Assess the morphology of the red blood cells.
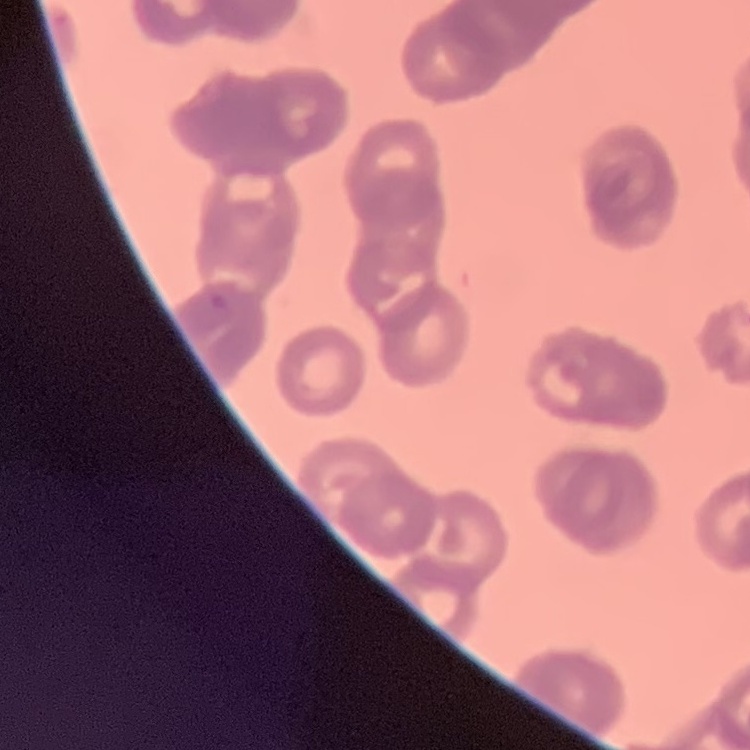

They show rouleaux formation.

Thin peripheral smear. One tile cut from a larger photomicrograph. Stained with either Field's or Giemsa.